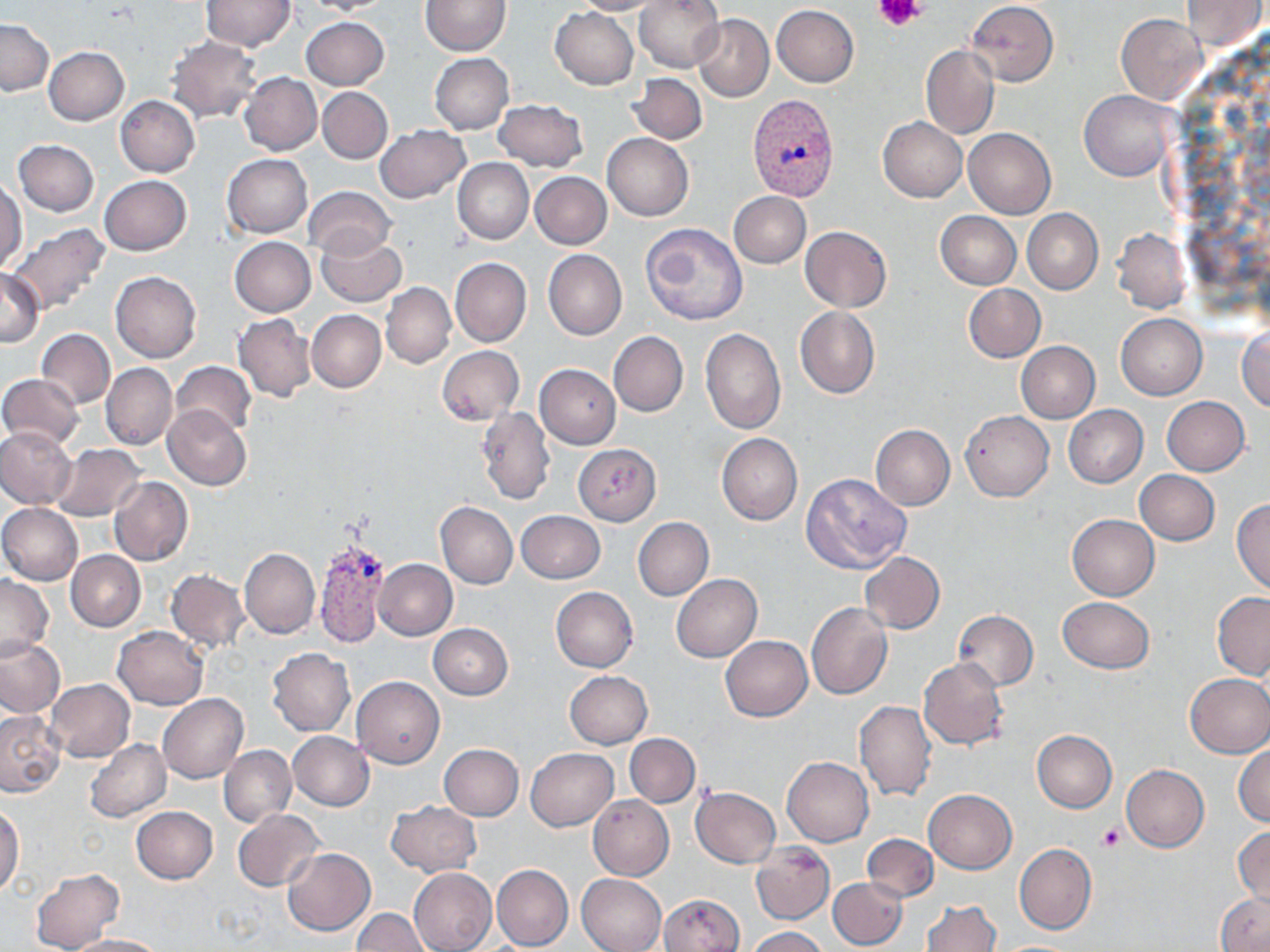

slide_level_diagnosis: Plasmodium vivax
preparation: thin blood smear
platelet_locations: 'approximate bounding boxes as (x1,y1)-(x2,y2) corner pairs in pixels: (874,0)-(925,31), (1096,822)-(1126,851)'
plasmodium_vivax_infected_red_blood_cell_locations: 'approximate bounding boxes as (x1,y1)-(x2,y2) corner pairs in pixels: (747,93)-(838,200), (313,537)-(388,650)'
image_size: 1270×952 pixels
stain: May-Grünwald-Giemsa
uninfected_red_blood_cell_locations: 'approximate bounding boxes as (x1,y1)-(x2,y2) corner pairs in pixels: (200,0)-(294,50), (302,0)-(394,15), (570,0)-(662,15), (634,0)-(724,73), (1182,0)-(1266,51), (419,1)-(510,55), (967,1)-(1059,86), (772,4)-(859,87), (550,6)-(639,89), (691,13)-(773,102), (1116,13)-(1208,104), (301,17)-(389,91), (0,19)-(53,95), (166,36)-(262,122), (42,46)-(129,125), (921,46)-(999,139), (431,53)-(513,133), (240,73)-(321,155), (628,73)-(707,145), (318,86)-(392,163), (1081,89)-(1179,181), (115,96)-(200,177), (493,98)-(588,170), (878,118)-(966,203), (374,124)-(470,202), (963,127)-(1056,220), (602,133)-(694,220), (12,139)-(99,215), (222,153)-(312,238), (454,158)-(533,245), (530,172)-(612,249), (99,175)-(192,256), (0,181)-(25,273), (304,186)-(395,260), (727,191)-(810,268), (1022,209)-(1102,294), (935,211)-(1021,289), (6,223)-(110,316), (640,223)-(747,327), (800,225)-(891,311), (1112,228)-(1191,313), (315,232)-(406,308), (230,237)-(316,316), (543,250)-(626,340), (450,257)-(532,346), (0,269)-(43,347), (111,271)-(201,362), (381,282)-(455,368), (964,284)-(1045,362), (795,307)-(879,399), (306,309)-(385,393), (233,313)-(317,401), (1116,313)-(1207,400), (1236,326)-(1269,412), (700,327)-(785,433), (36,328)-(115,408), (608,332)-(687,417), (1016,341)-(1100,423), (436,345)-(523,425), (171,361)-(257,437), (101,363)-(177,450), (534,364)-(621,448), (0,374)-(85,449), (1162,397)-(1250,476), (163,405)-(251,490), (1064,405)-(1148,488), (477,406)-(555,506), (960,410)-(1053,501), (869,424)-(955,510), (0,427)-(77,509), (716,433)-(802,526), (51,443)-(146,521), (573,444)-(661,525), (1134,470)-(1219,545), (801,472)-(911,574), (108,476)-(193,567), (1232,498)-(1270,595), (435,501)-(518,589), (0,503)-(83,585), (516,510)-(605,583), (1067,514)-(1159,600), (633,517)-(714,600), (239,549)-(320,639), (66,551)-(145,631), (859,552)-(945,634), (374,559)-(457,640), (166,569)-(251,652), (0,574)-(53,660), (671,574)-(762,661), (550,587)-(638,672), (1212,592)-(1270,680), (1057,596)-(1154,673), (806,602)-(892,701), (952,610)-(1038,690), (428,624)-(513,699), (113,626)-(208,709), (0,635)-(67,718), (721,635)-(812,721), (267,649)-(356,736), (918,657)-(1009,750), (564,671)-(652,749), (1183,672)-(1270,758), (352,676)-(445,769), (46,678)-(134,762), (157,693)-(248,783), (854,701)-(936,801), (0,708)-(67,797), (287,731)-(374,810), (1032,731)-(1117,812), (625,734)-(700,807), (84,740)-(171,822), (1233,742)-(1270,827), (438,744)-(523,820), (219,745)-(296,828), (526,748)-(618,831), (782,756)-(873,847), (1121,764)-(1208,852), (691,786)-(780,867), (924,789)-(1016,873), (588,795)-(673,880), (386,799)-(481,877), (0,803)-(24,897), (131,806)-(218,884), (232,810)-(324,891), (1233,824)-(1269,906), (862,834)-(939,902), (1014,843)-(1096,934), (751,844)-(834,925), (283,848)-(375,936), (491,864)-(573,952), (29,867)-(124,952), (409,867)-(496,952), (577,873)-(667,952), (828,877)-(908,950), (1217,891)-(1270,952), (658,893)-(744,952), (922,899)-(1000,952), (352,909)-(429,951), (746,926)-(828,952), (68,934)-(166,952)'
field_of_view: one of a larger specimen
modality: optical microscopy
magnification: 1000x